Point out leukocytes.
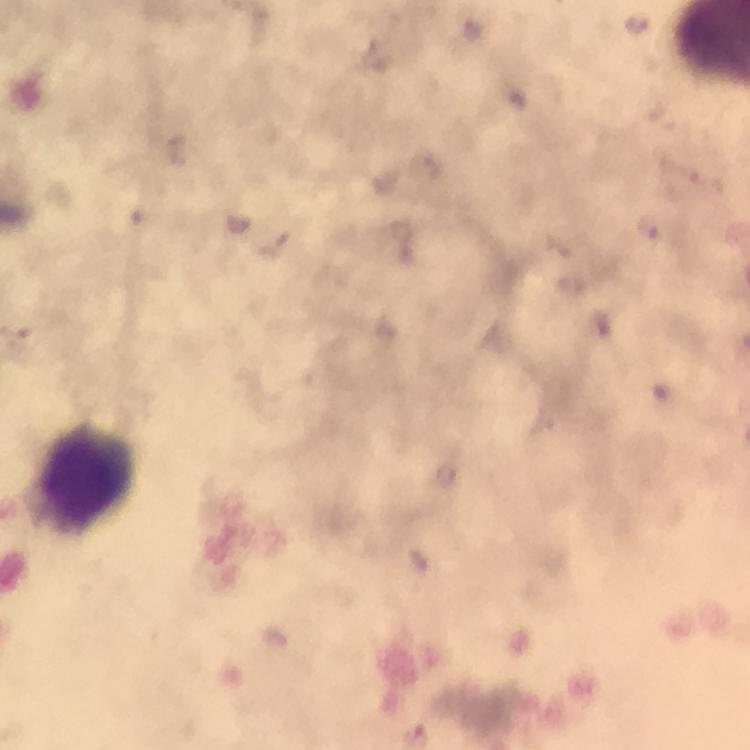

Approximate object centers, in pixels from the top-left corner.
Leukocytes: (x=78, y=481).

Summary:
  - Plasmodium parasite locations: (x=638, y=23), (x=647, y=227)
  - Context: from a malaria diagnostic workup
  - Image size: 750×750 pixels
  - Immersion oil: applied
  - Cropped from: a single field of view
  - Stain: Giemsa
  - Capture: smartphone photograph through a microscope
  - Magnification: 100x
  - Preparation: thick blood film